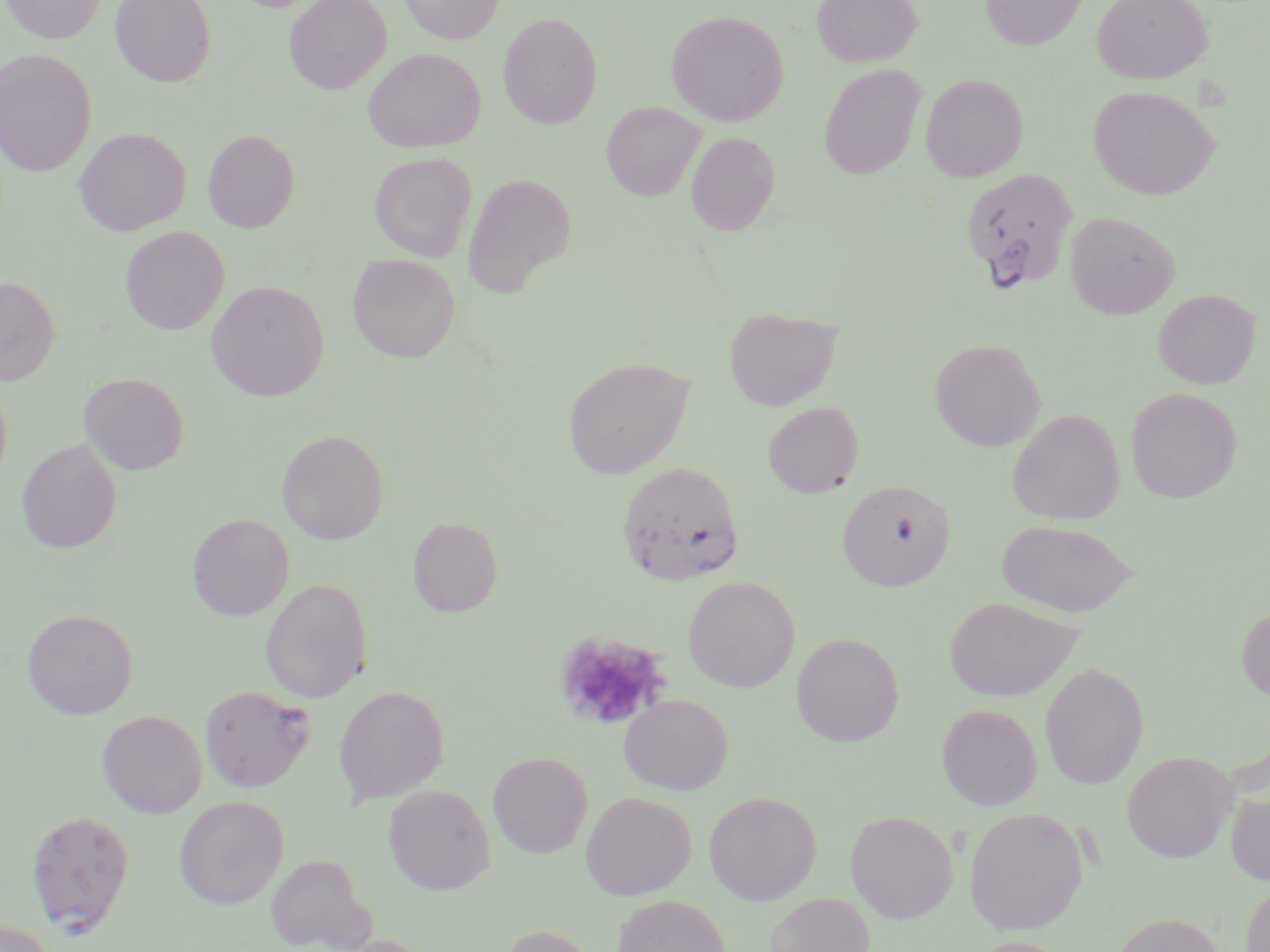

Summary:
  - Coordinate format: approximate bounding boxes as named x1/y1/x2/y2 corners in pixels
  - Uninfected red blood cell locations: (x1=2, y1=0, x2=106, y2=43), (x1=110, y1=0, x2=216, y2=87), (x1=284, y1=0, x2=391, y2=94), (x1=400, y1=0, x2=504, y2=44), (x1=811, y1=0, x2=922, y2=67), (x1=980, y1=0, x2=1087, y2=50), (x1=1092, y1=0, x2=1212, y2=84), (x1=666, y1=10, x2=789, y2=126), (x1=498, y1=12, x2=603, y2=129), (x1=0, y1=48, x2=97, y2=177), (x1=363, y1=48, x2=485, y2=152), (x1=818, y1=64, x2=927, y2=180), (x1=920, y1=73, x2=1028, y2=181), (x1=1088, y1=85, x2=1220, y2=200), (x1=601, y1=101, x2=705, y2=201), (x1=74, y1=127, x2=191, y2=235), (x1=203, y1=129, x2=300, y2=232), (x1=686, y1=132, x2=780, y2=235), (x1=369, y1=152, x2=477, y2=262), (x1=463, y1=173, x2=577, y2=295), (x1=1064, y1=211, x2=1180, y2=319), (x1=120, y1=226, x2=229, y2=335), (x1=348, y1=254, x2=461, y2=362), (x1=0, y1=275, x2=62, y2=385), (x1=207, y1=280, x2=330, y2=401), (x1=1153, y1=289, x2=1260, y2=388), (x1=724, y1=307, x2=843, y2=410), (x1=929, y1=338, x2=1046, y2=451), (x1=563, y1=356, x2=694, y2=478), (x1=79, y1=372, x2=189, y2=475), (x1=0, y1=379, x2=13, y2=490), (x1=1125, y1=387, x2=1242, y2=503), (x1=763, y1=402, x2=863, y2=497), (x1=1007, y1=409, x2=1125, y2=524), (x1=277, y1=430, x2=388, y2=544), (x1=17, y1=439, x2=122, y2=553), (x1=837, y1=480, x2=955, y2=591), (x1=187, y1=513, x2=294, y2=621), (x1=409, y1=516, x2=502, y2=618), (x1=997, y1=518, x2=1140, y2=617), (x1=683, y1=576, x2=799, y2=692), (x1=260, y1=578, x2=372, y2=703), (x1=944, y1=596, x2=1083, y2=702), (x1=1236, y1=604, x2=1270, y2=702), (x1=23, y1=609, x2=139, y2=718), (x1=791, y1=632, x2=904, y2=747), (x1=1039, y1=661, x2=1148, y2=790), (x1=333, y1=685, x2=450, y2=805), (x1=620, y1=694, x2=733, y2=794), (x1=936, y1=704, x2=1041, y2=810), (x1=97, y1=710, x2=207, y2=818), (x1=1121, y1=750, x2=1237, y2=862), (x1=488, y1=751, x2=593, y2=857), (x1=383, y1=784, x2=496, y2=894), (x1=1225, y1=788, x2=1270, y2=886), (x1=580, y1=790, x2=697, y2=900), (x1=703, y1=790, x2=822, y2=905), (x1=174, y1=795, x2=289, y2=909), (x1=964, y1=807, x2=1087, y2=936), (x1=845, y1=810, x2=958, y2=923), (x1=265, y1=853, x2=375, y2=951), (x1=1240, y1=881, x2=1270, y2=952), (x1=764, y1=892, x2=875, y2=952), (x1=612, y1=895, x2=731, y2=952), (x1=1111, y1=912, x2=1224, y2=952), (x1=0, y1=919, x2=58, y2=952), (x1=499, y1=924, x2=600, y2=952), (x1=962, y1=936, x2=1072, y2=952)
  - Platelet locations: (x1=554, y1=630, x2=670, y2=730)
  - Plasmodium falciparum-infected red blood cell locations: (x1=959, y1=168, x2=1079, y2=293), (x1=616, y1=461, x2=745, y2=587), (x1=199, y1=684, x2=314, y2=792), (x1=24, y1=810, x2=136, y2=934)
  - Slide-level diagnosis: Plasmodium falciparum
  - Magnification: 1000x
  - Image size: 1270×952 pixels
  - Modality: light microscopy
  - Field of view: single
  - Preparation: thin blood film
  - Stain: May-Grünwald-Giemsa